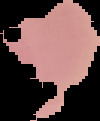
malaria status = uninfected
preparation = thin blood film
image type = segmented cell region on a black background
image size = 100×121 pixels